Locate every uninfected red blood cell.
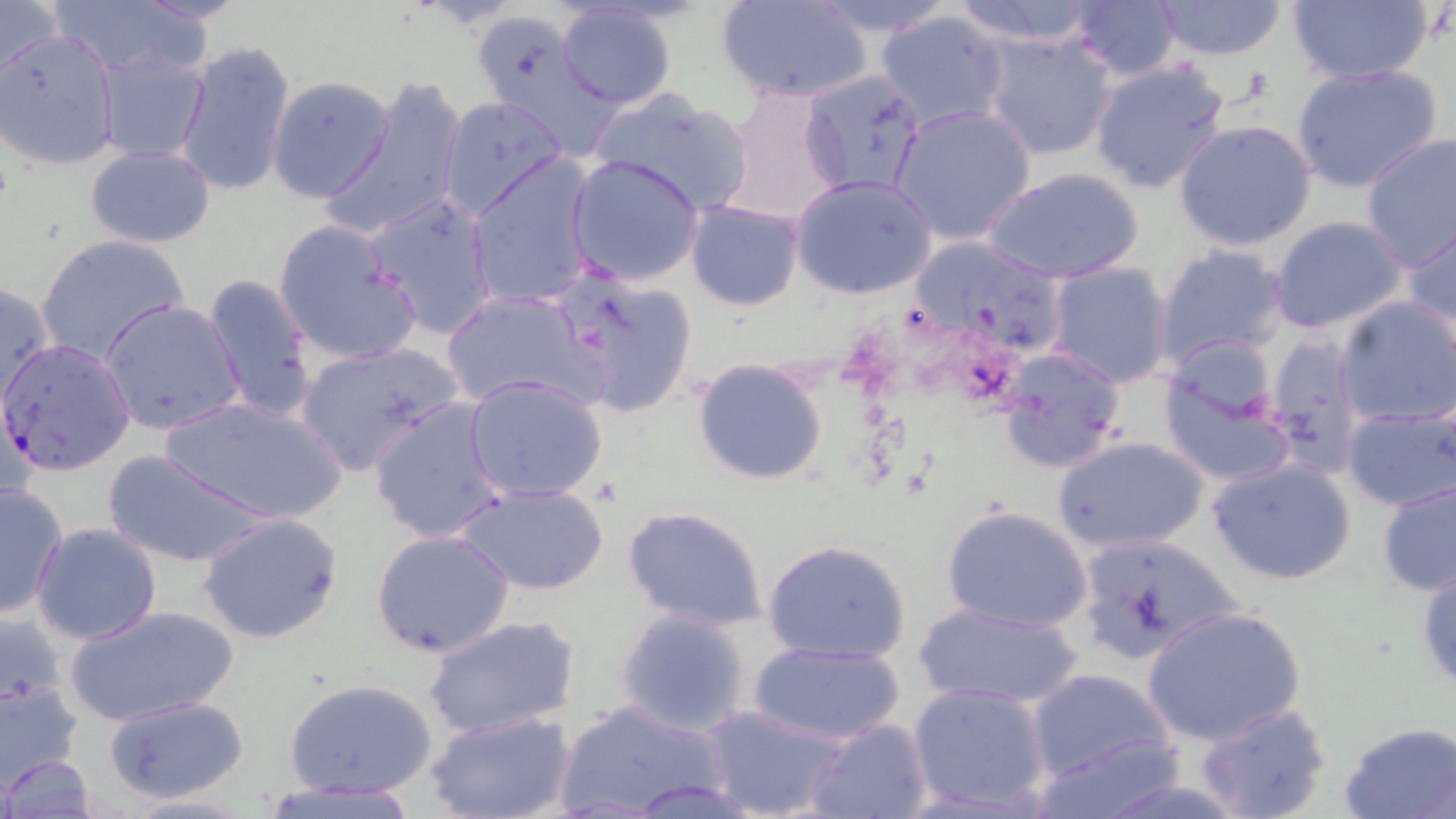
Approximate bounding boxes as (x1,y1)-(x2,y2) corner pairs in pixels.
Uninfected red blood cells: (0,0)-(66,85), (718,0)-(871,103), (802,0)-(956,38), (949,0)-(1101,46), (1062,0)-(1184,84), (1151,0)-(1289,61), (1282,0)-(1435,86), (47,1)-(202,77), (554,4)-(677,110), (875,8)-(1012,131), (473,13)-(610,148), (0,30)-(120,170), (981,30)-(1116,162), (176,40)-(296,199), (95,43)-(211,162), (1087,59)-(1233,197), (1288,64)-(1444,195), (798,70)-(927,199), (265,76)-(395,204), (323,80)-(468,241), (716,85)-(848,224), (587,87)-(755,217), (438,95)-(568,220), (890,103)-(1037,246), (1172,119)-(1318,252), (1358,135)-(1455,270), (84,144)-(217,248), (567,154)-(706,287), (467,157)-(599,310), (984,165)-(1144,283), (792,175)-(936,299), (363,191)-(499,339), (685,199)-(803,311), (1269,214)-(1406,335), (1403,219)-(1456,338), (272,222)-(420,365), (1154,230)-(1409,351), (33,233)-(192,368), (1152,244)-(1290,369), (1046,262)-(1175,389), (550,268)-(699,417), (200,271)-(318,423), (0,282)-(58,411), (441,288)-(601,411), (1335,296)-(1456,427), (98,298)-(241,435), (1264,334)-(1365,475), (292,341)-(464,475), (995,347)-(1128,475), (1157,350)-(1295,489), (693,358)-(829,486), (464,375)-(609,504), (161,395)-(347,526), (368,397)-(508,545), (1339,402)-(1455,514), (1051,434)-(1211,555), (102,450)-(270,568), (1206,456)-(1360,588), (1377,476)-(1456,598), (0,482)-(69,617), (457,483)-(609,597), (621,504)-(771,632), (942,504)-(1095,634), (198,512)-(346,646), (31,523)-(163,645), (369,530)-(517,659), (1071,533)-(1242,667), (763,538)-(915,665), (1416,556)-(1456,699), (912,601)-(1089,712), (63,603)-(240,727), (1140,604)-(1308,747), (1,607)-(67,711), (615,610)-(751,737), (425,614)-(582,739), (748,641)-(905,746), (1024,667)-(1176,788), (0,673)-(85,790), (282,676)-(439,801), (907,682)-(1053,815), (102,694)-(251,804), (554,700)-(729,817), (1192,702)-(1333,819), (700,704)-(849,819), (425,710)-(572,819), (800,716)-(932,819), (1338,721)-(1456,818), (1027,734)-(1186,819), (2,756)-(102,819), (257,778)-(427,818).

{
  "slide_level_diagnosis": "Plasmodium falciparum",
  "preparation": "thin blood smear",
  "magnification": "1000x",
  "stain": "May-Grünwald-Giemsa",
  "image_size": "1456×819 pixels",
  "plasmodium_falciparum_infected_red_blood_cell_locations": "approximate bounding boxes as (x1,y1)-(x2,y2) corner pairs in pixels: (907,236)-(1073,362), (0,337)-(137,475)",
  "modality": "optical microscopy",
  "field_of_view": "single"
}